Evaluate for malaria.
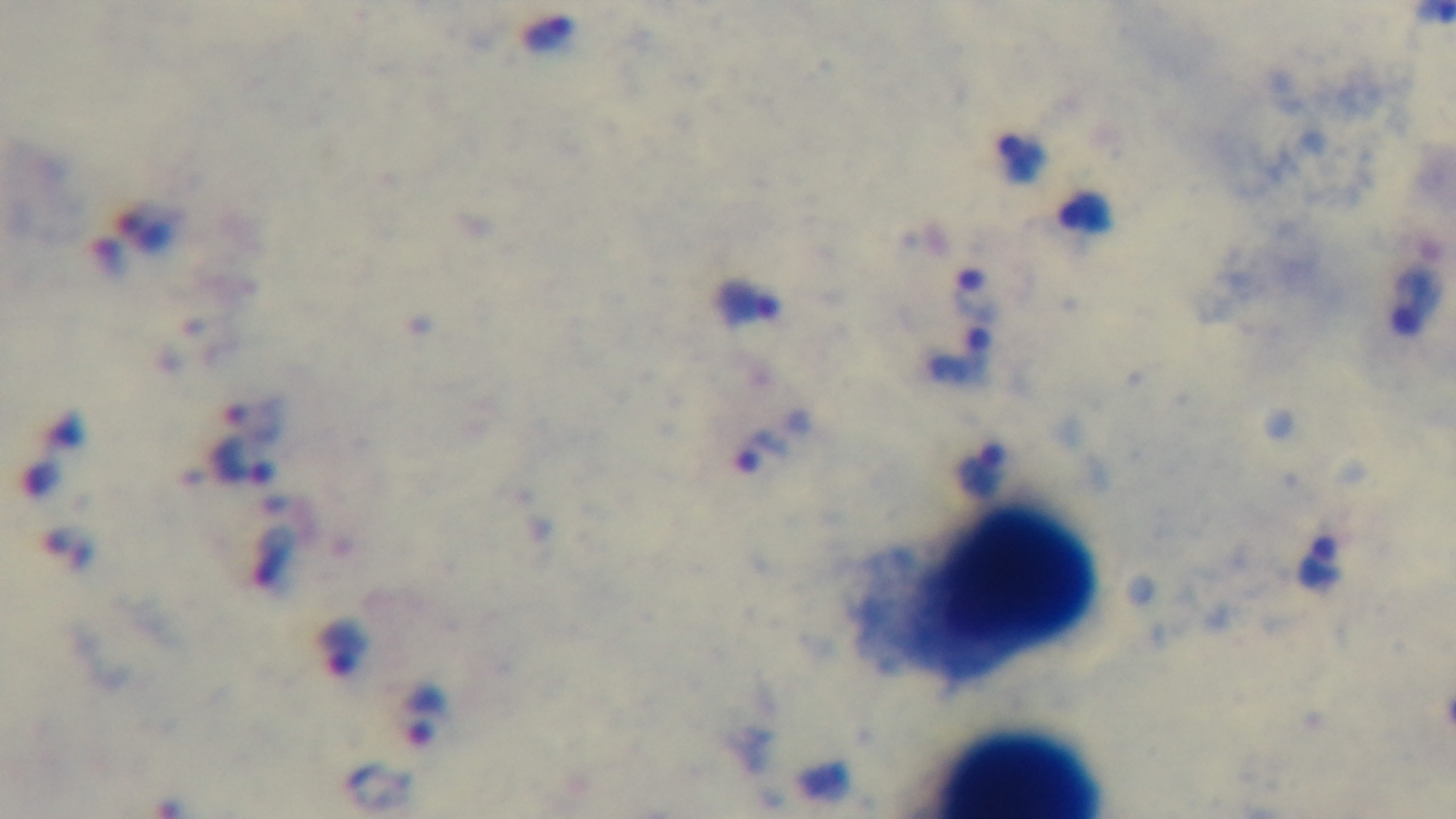

Infected.

Single field of view. 100x oil-immersion objective. Giemsa-stained. Preparation: thick blood film. Photomicrograph. Captured with a mounted 4K digital camera.